Describe the morphology of the erythrocytes.
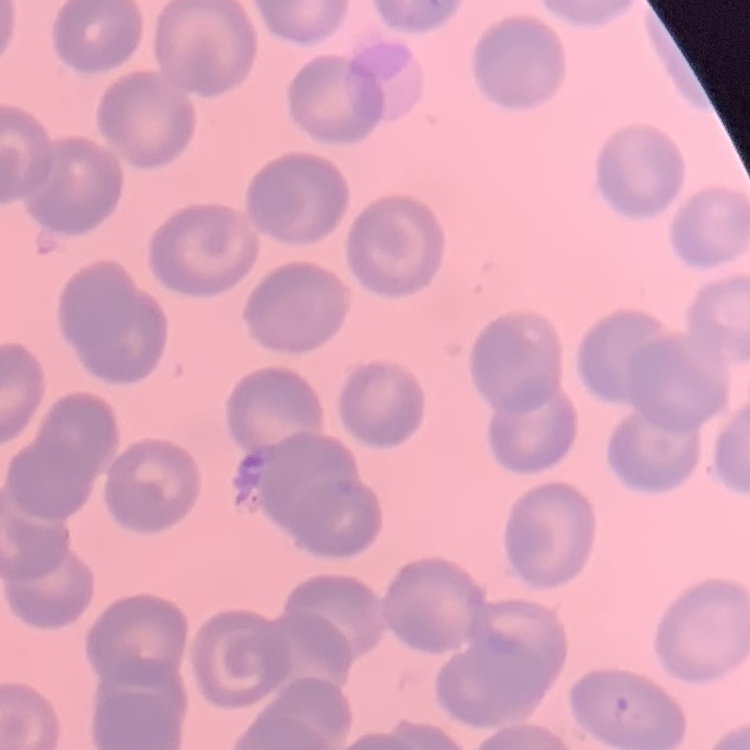

They show no rouleaux formation.

Summary:
  - Preparation: thin blood film
  - Image type: square crop of a larger photomicrograph
  - Stain: Field's or Giemsa